Locate and identify every blood parasite.
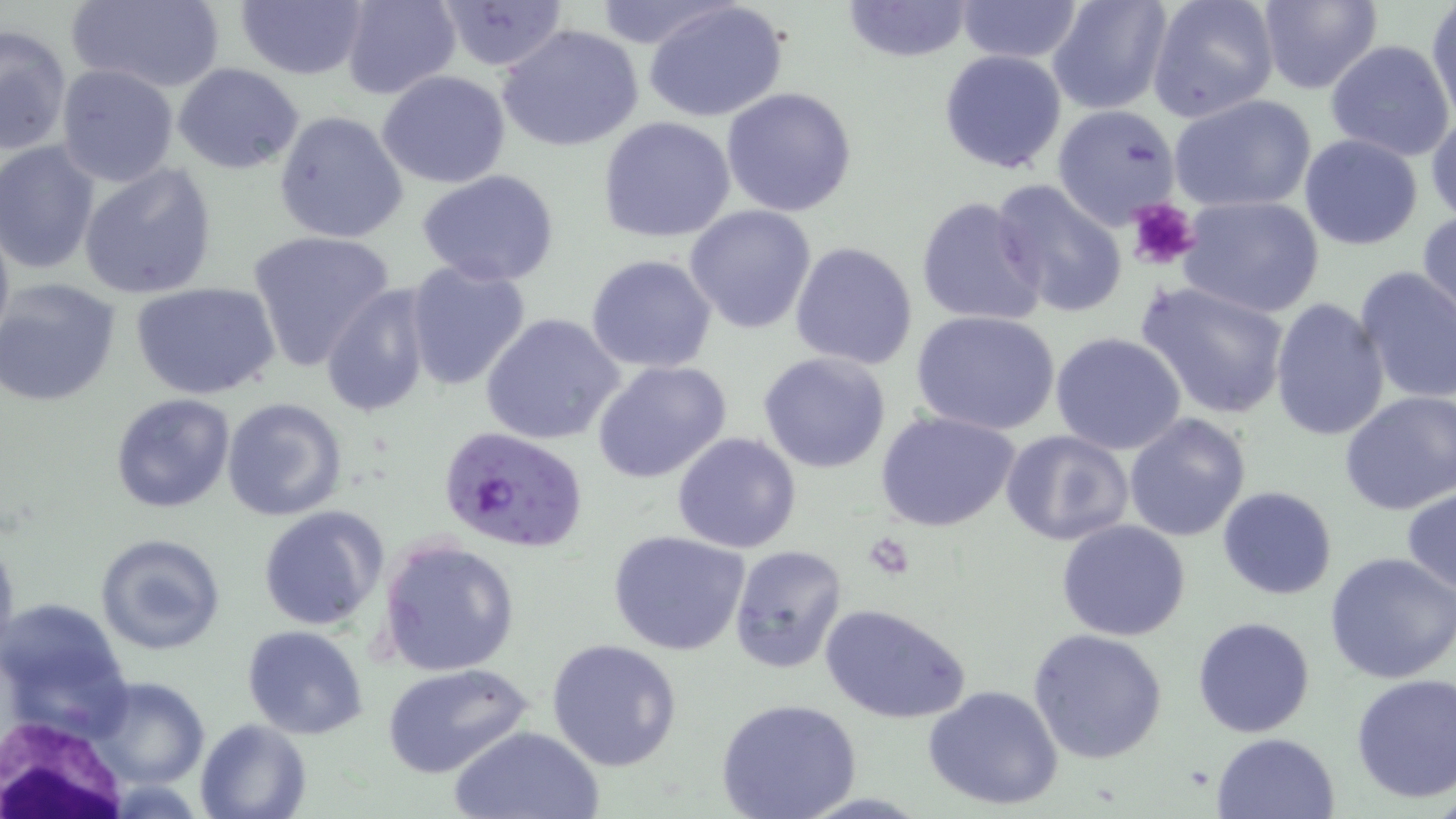

Approximate bounding boxes as named x1/y1/x2/y2 corners in pixels.
Plasmodium falciparum-infected red blood cells: (x1=442, y1=424, x2=592, y2=554).
No Plasmodium ovale, Plasmodium malariae, Plasmodium vivax, Babesia divergens, or Trypanosoma brucei observed.

Uninfected red blood cell locations: (x1=64, y1=0, x2=225, y2=92), (x1=338, y1=0, x2=462, y2=101), (x1=429, y1=0, x2=569, y2=72), (x1=587, y1=0, x2=733, y2=52), (x1=839, y1=0, x2=975, y2=63), (x1=954, y1=0, x2=1085, y2=62), (x1=1047, y1=0, x2=1173, y2=114), (x1=1147, y1=0, x2=1281, y2=123), (x1=1257, y1=0, x2=1384, y2=95), (x1=234, y1=1, x2=368, y2=80), (x1=643, y1=1, x2=788, y2=123), (x1=1428, y1=1, x2=1456, y2=125), (x1=497, y1=24, x2=643, y2=152), (x1=1, y1=25, x2=71, y2=156), (x1=1325, y1=39, x2=1455, y2=160), (x1=939, y1=48, x2=1069, y2=175), (x1=172, y1=62, x2=304, y2=174), (x1=56, y1=64, x2=179, y2=186), (x1=376, y1=71, x2=512, y2=189), (x1=721, y1=87, x2=857, y2=217), (x1=1168, y1=93, x2=1318, y2=214), (x1=1052, y1=105, x2=1181, y2=227), (x1=274, y1=109, x2=408, y2=246), (x1=1426, y1=111, x2=1456, y2=226), (x1=597, y1=116, x2=735, y2=243), (x1=1298, y1=133, x2=1424, y2=250), (x1=0, y1=141, x2=100, y2=274), (x1=79, y1=163, x2=218, y2=299), (x1=416, y1=169, x2=561, y2=287), (x1=988, y1=180, x2=1127, y2=318), (x1=915, y1=195, x2=1046, y2=327), (x1=1180, y1=195, x2=1325, y2=318), (x1=686, y1=205, x2=819, y2=335), (x1=1416, y1=208, x2=1455, y2=326), (x1=0, y1=211, x2=14, y2=354), (x1=245, y1=229, x2=397, y2=372), (x1=790, y1=241, x2=919, y2=370), (x1=585, y1=254, x2=717, y2=374), (x1=404, y1=260, x2=531, y2=391), (x1=1353, y1=266, x2=1456, y2=403), (x1=0, y1=278, x2=122, y2=410), (x1=1137, y1=280, x2=1291, y2=419), (x1=131, y1=281, x2=281, y2=402), (x1=319, y1=284, x2=436, y2=420), (x1=1268, y1=298, x2=1390, y2=442), (x1=911, y1=309, x2=1061, y2=435), (x1=480, y1=312, x2=626, y2=447), (x1=1048, y1=333, x2=1188, y2=457), (x1=758, y1=351, x2=891, y2=475), (x1=591, y1=359, x2=732, y2=484), (x1=1337, y1=390, x2=1455, y2=514), (x1=109, y1=393, x2=234, y2=513), (x1=221, y1=397, x2=347, y2=521), (x1=876, y1=410, x2=1022, y2=533), (x1=1123, y1=412, x2=1251, y2=542), (x1=999, y1=429, x2=1134, y2=546), (x1=671, y1=431, x2=802, y2=553), (x1=1218, y1=486, x2=1337, y2=600), (x1=1401, y1=486, x2=1456, y2=598), (x1=258, y1=505, x2=388, y2=631), (x1=1056, y1=521, x2=1192, y2=642), (x1=606, y1=530, x2=752, y2=657), (x1=96, y1=532, x2=226, y2=654), (x1=0, y1=533, x2=19, y2=655), (x1=377, y1=536, x2=522, y2=677), (x1=727, y1=544, x2=847, y2=672), (x1=1325, y1=552, x2=1455, y2=684), (x1=1, y1=597, x2=135, y2=736), (x1=819, y1=602, x2=970, y2=725), (x1=1192, y1=615, x2=1316, y2=738), (x1=241, y1=625, x2=369, y2=740), (x1=1029, y1=627, x2=1170, y2=765), (x1=545, y1=638, x2=683, y2=771), (x1=382, y1=663, x2=531, y2=778), (x1=1350, y1=673, x2=1456, y2=805), (x1=85, y1=675, x2=214, y2=789), (x1=923, y1=683, x2=1065, y2=812), (x1=716, y1=699, x2=862, y2=819), (x1=194, y1=718, x2=311, y2=819), (x1=446, y1=725, x2=604, y2=819), (x1=1212, y1=731, x2=1341, y2=819). Platelet locations: (x1=1126, y1=199, x2=1201, y2=271), (x1=867, y1=532, x2=913, y2=578). White blood cell locations: (x1=1, y1=719, x2=159, y2=816). Slide-level diagnosis: Plasmodium falciparum. One field of a larger specimen. 1000x magnification. May-Grünwald-Giemsa stain. Thin blood film. Optical microscopy. Image is 1456×819 pixels.